State which parasite is depicted.
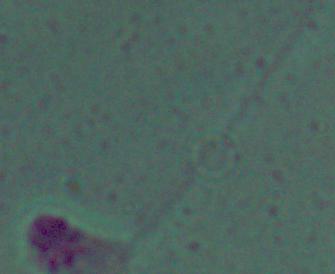

Leishmania.

Summary:
  - Modality: photomicrograph
  - Magnification: 1000x